Assess this cell for malaria.
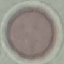
Uninfected.

Cell patch, automatically extracted from a larger field of view and resized to 64 × 64 pixels. Acquired by smartphone through the microscope eyepiece. Thin blood film. Giemsa-stained preparation.